Identify the parasite.
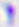

Toxoplasma gondii.

magnification = 400x
modality = photomicrograph